State which parasite is depicted.
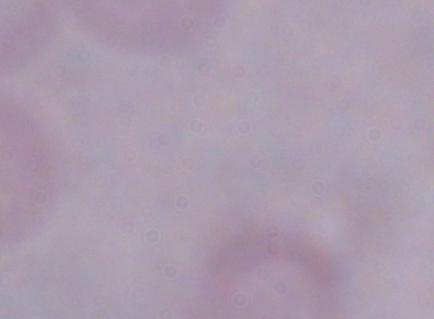
A trypanosome.

Captured at 1000x magnification. Photomicrograph.